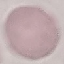
malaria_status: uninfected
stain: Giemsa
image_type: cell patch, automatically extracted from a larger field of view and resized to 64 × 64 pixels
capture: smartphone through the microscope eyepiece
preparation: thin blood smear